Comment on the morphology of the erythrocytes.
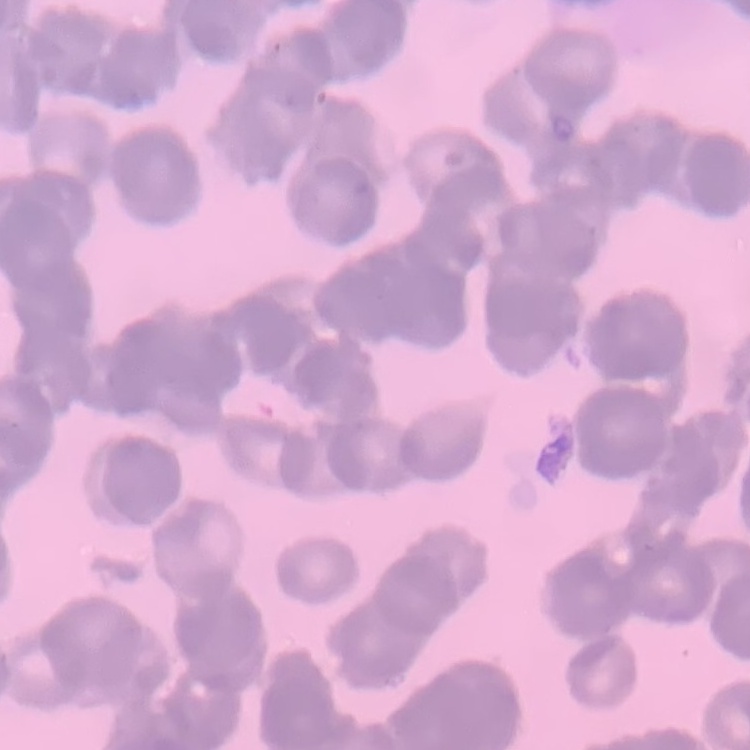
Rouleaux formation.

Stained with either Field's or Giemsa. Thin blood film. One tile cut from a larger photomicrograph.